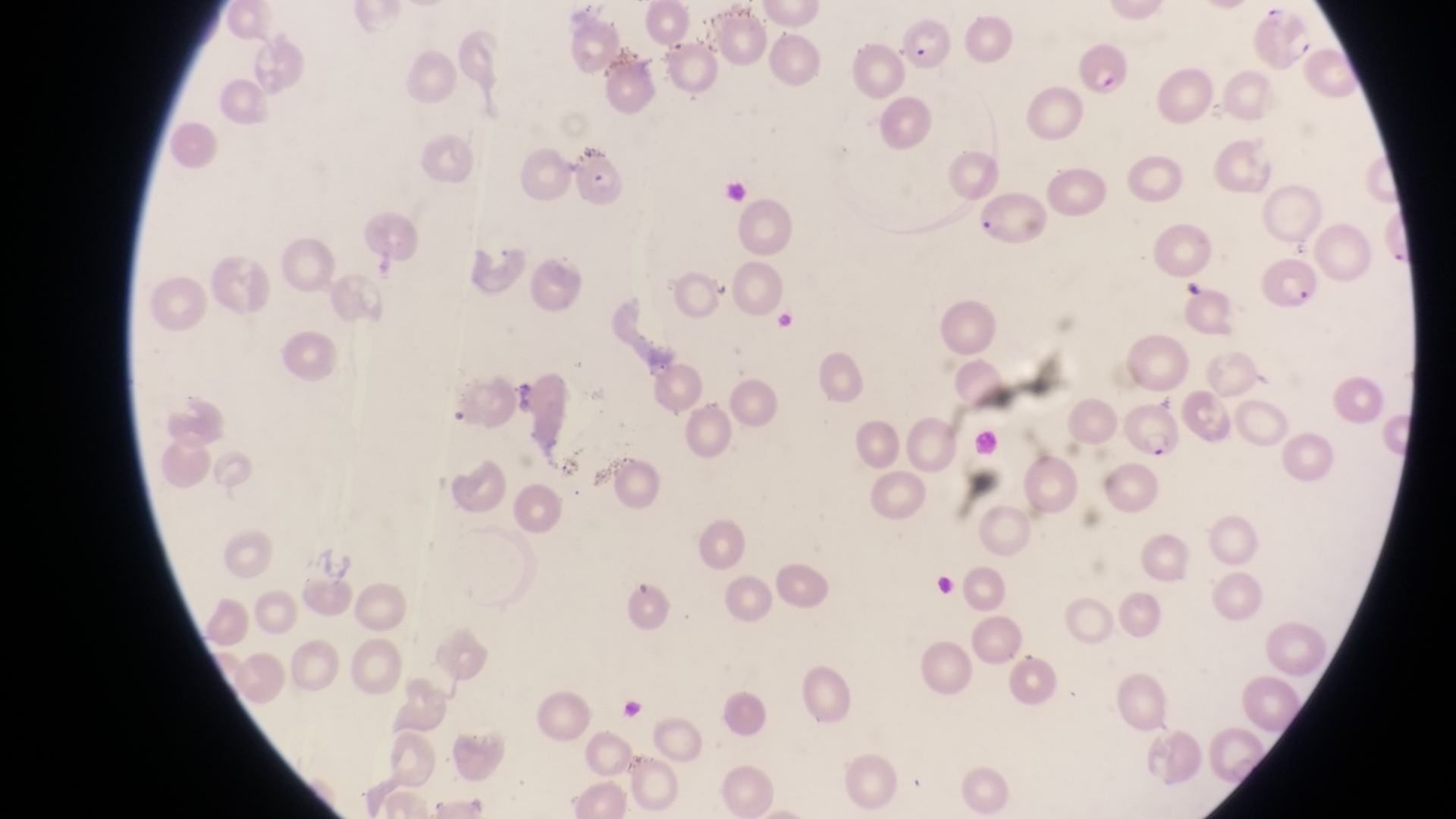
magnification = 1000x
image size = 1456×819 pixels
preparation = thin blood film
capture = smartphone photograph through the eyepiece of an Olympus CX-23 microscope
parasitised red blood cell locations = approximate bounding boxes as (left, top, right, bottom) in pixels: (898, 16, 961, 71), (1081, 37, 1134, 100), (573, 146, 628, 204), (981, 185, 1052, 257), (1257, 253, 1321, 316), (1122, 400, 1186, 459)
country = Uganda
field of view = single